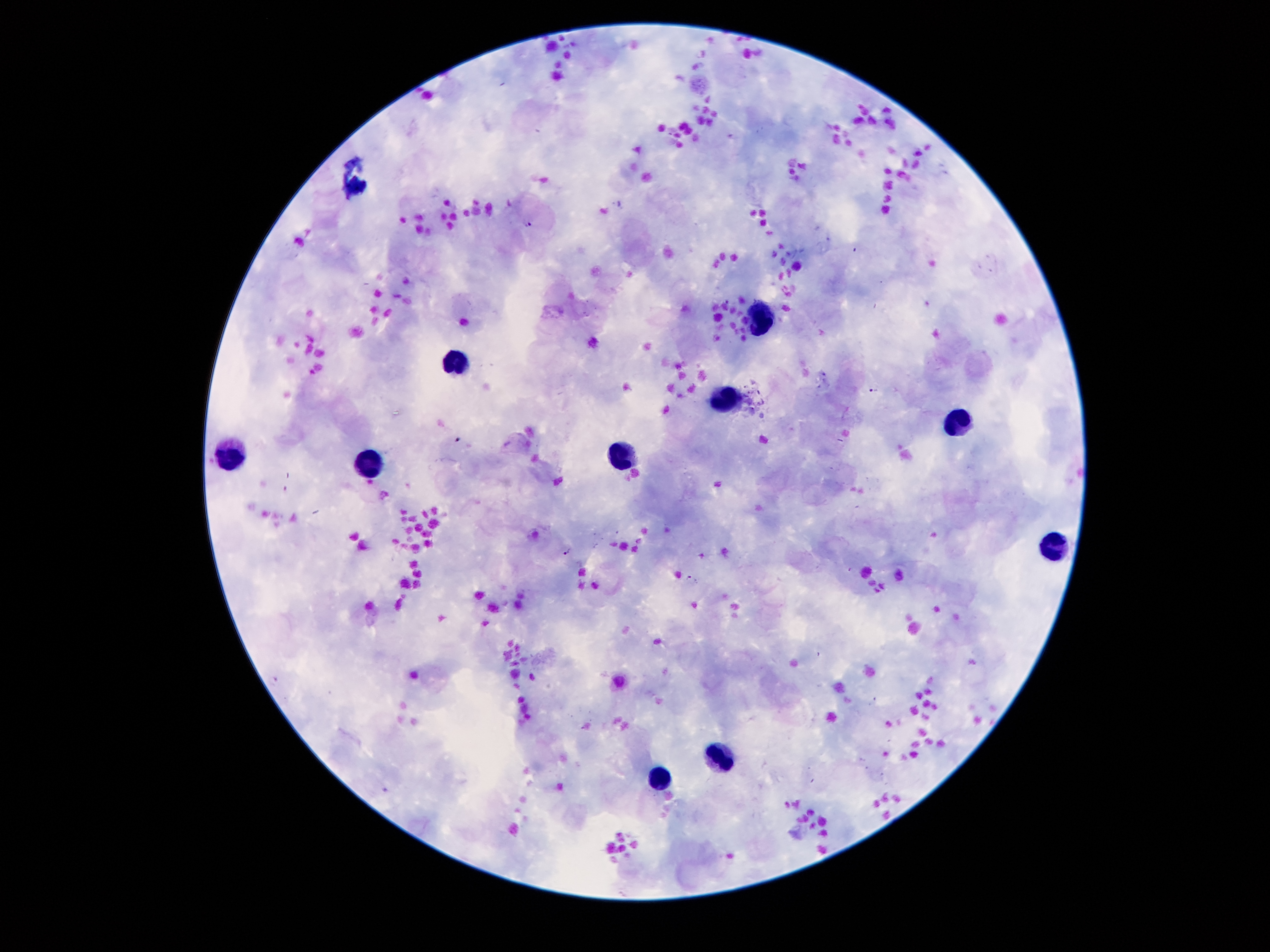

Approximate centers as [x, y] in pixels.
Summary:
  - Leukocyte locations: [758, 317], [458, 362], [726, 392], [961, 414], [227, 456], [624, 456], [366, 462], [1055, 542], [724, 759], [654, 780]
  - Plasmodium parasite locations: [526, 222], [874, 390], [460, 439], [567, 551], [691, 579]
  - Stain: Giemsa
  - Field of view: single
  - Patient malaria status: infected with Plasmodium falciparum
  - Capture: smartphone camera through the microscope eyepiece
  - Image size: 1270×952 pixels
  - Magnification: 100x
  - Preparation: thick peripheral-blood smear